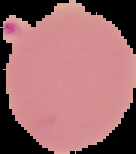

{
  "image_size": "136×154 pixels",
  "image_type": "segmented cell region on a black background",
  "result": "Plasmodium parasites detected",
  "preparation": "thin blood smear"
}